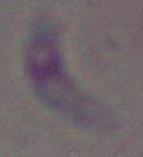 Captured at 1000x magnification. Toxoplasma gondii is seen. Micrograph.